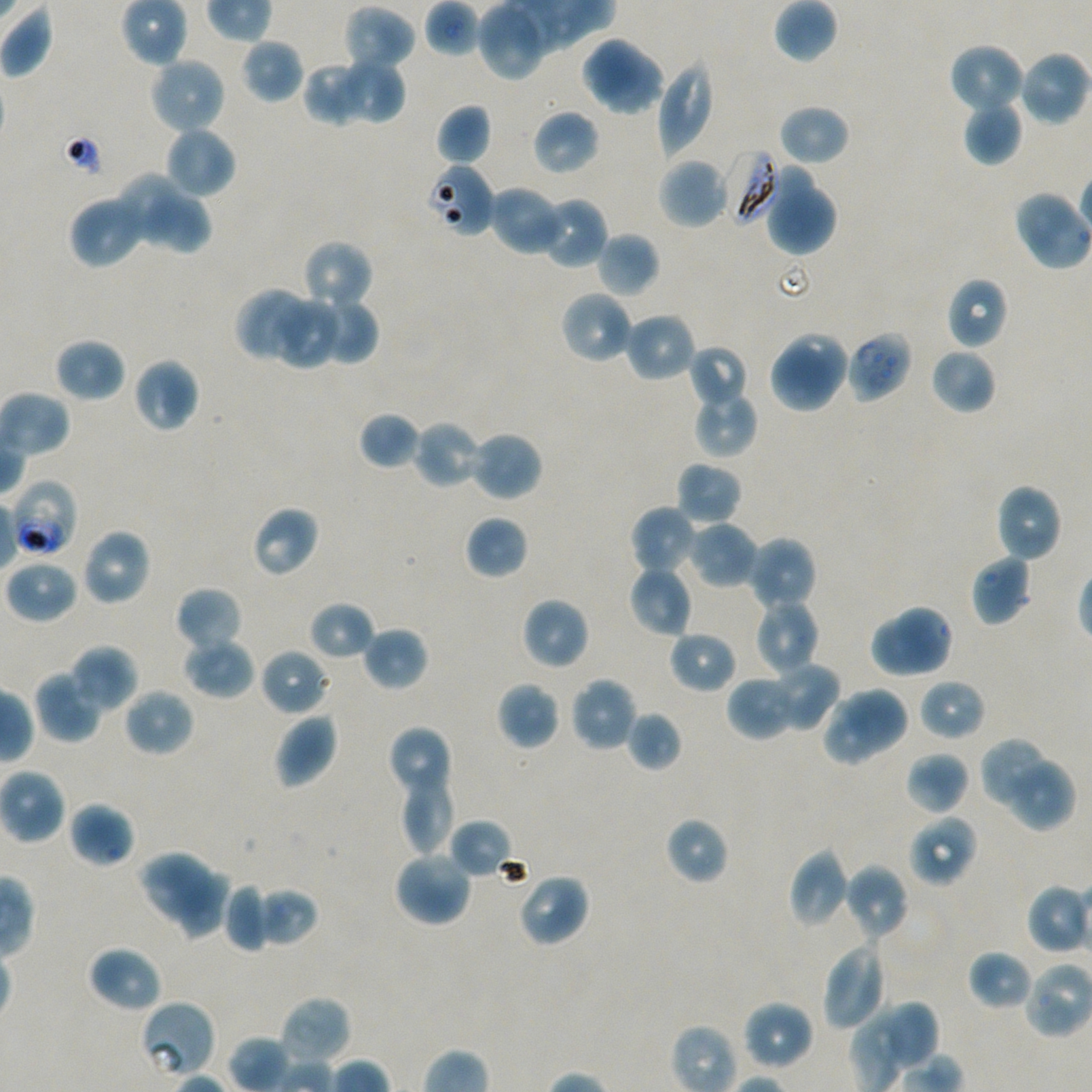
Not every red blood cell is marked. A life-cycle stage — or a range of stages, where the recorded stages span more than one — follows each staged infected red blood cell.
locations_of_infected_red_blood_cells: 'approximate bounding boxes as {x1, y1, x2, y2} in pixels: {724, 149, 781, 224}; {846, 330, 912, 402}; {10, 479, 77, 559} early trophozoite to early schizont'
preparation: thin blood film
locations_of_red_blood_cells_of_indeterminate_infection_status: 'approximate bounding boxes as {x1, y1, x2, y2} in pixels: {426, 162, 496, 237}, {139, 999, 218, 1079}'
stain: Giemsa
objective: 100x, oil immersion, numerical aperture 1.45
locations_of_uninfected_red_blood_cells: 'approximate bounding boxes as {x1, y1, x2, y2} in pixels: {478, 0, 549, 81}, {344, 5, 416, 72}, {579, 35, 641, 103}, {240, 37, 305, 103}, {948, 43, 1025, 116}, {1017, 50, 1089, 127}, {598, 51, 666, 115}, {148, 55, 228, 134}, {334, 58, 406, 125}, {656, 58, 715, 158}, {303, 62, 371, 126}, {964, 100, 1024, 166}, {435, 104, 492, 166}, {779, 104, 850, 166}, {532, 109, 600, 175}, {163, 126, 236, 199}, {657, 157, 727, 229}, {770, 164, 816, 234}, {118, 172, 184, 247}, {488, 185, 566, 257}, {770, 189, 837, 256}, {1013, 189, 1074, 253}, {68, 193, 147, 269}, {154, 193, 213, 256}, {539, 196, 609, 270}, {596, 231, 659, 297}, {302, 240, 374, 311}, {946, 276, 1008, 350}, {234, 287, 308, 359}, {559, 289, 634, 365}, {311, 295, 379, 365}, {275, 298, 337, 367}, {623, 312, 696, 383}, {778, 330, 848, 401}, {54, 337, 126, 402}, {687, 344, 748, 410}, {767, 344, 835, 415}, {930, 348, 997, 415}, {132, 357, 200, 433}, {692, 389, 758, 458}, {358, 411, 421, 470}, {413, 418, 485, 489}, {469, 430, 543, 503}, {676, 460, 742, 526}, {994, 484, 1063, 563}, {251, 505, 319, 578}, {630, 505, 697, 575}, {465, 515, 529, 580}, {687, 520, 759, 589}, {81, 528, 151, 606}, {746, 536, 818, 612}, {970, 553, 1032, 627}, {4, 559, 79, 623}, {627, 565, 693, 639}, {175, 586, 243, 654}, {521, 597, 589, 670}, {753, 598, 820, 676}, {308, 601, 375, 661}, {892, 605, 953, 674}, {868, 619, 935, 679}, {361, 625, 429, 691}, {668, 630, 738, 693}, {182, 636, 255, 699}, {69, 644, 137, 711}, {260, 648, 331, 716}, {769, 661, 841, 732}, {33, 670, 102, 742}, {726, 675, 797, 741}, {569, 676, 638, 752}, {918, 678, 986, 741}, {496, 681, 560, 750}, {843, 685, 911, 752}, {123, 688, 195, 757}, {823, 695, 883, 766}, {625, 710, 682, 771}, {273, 711, 339, 788}, {386, 725, 452, 799}, {983, 740, 1045, 805}, {905, 750, 969, 815}, {1009, 759, 1074, 831}, {399, 772, 457, 854}, {69, 801, 135, 867}, {908, 814, 978, 887}, {665, 816, 729, 884}, {448, 818, 514, 879}, {788, 848, 851, 928}, {138, 850, 216, 923}, {393, 850, 472, 927}, {843, 864, 909, 941}, {176, 867, 235, 946}, {517, 873, 590, 948}, {223, 884, 270, 952}, {255, 887, 319, 947}, {821, 940, 888, 1031}, {86, 945, 162, 1013}, {967, 949, 1034, 1011}, {1025, 961, 1092, 1039}, {279, 994, 351, 1065}, {742, 999, 814, 1072}, {887, 1001, 940, 1070}'
image_size: 1092×1092 pixels
field_of_view: single
donor_blood_group: A+/O+
culture: in-vitro Plasmodium falciparum strain NF54, static